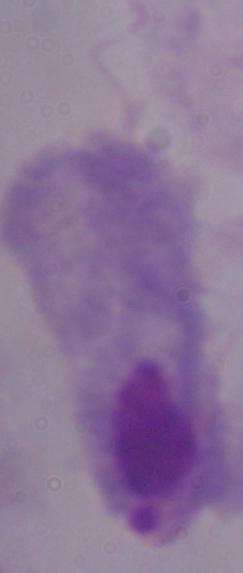
Summary:
  - Modality: micrograph
  - Identification: trichomonad
  - Magnification: 1000x